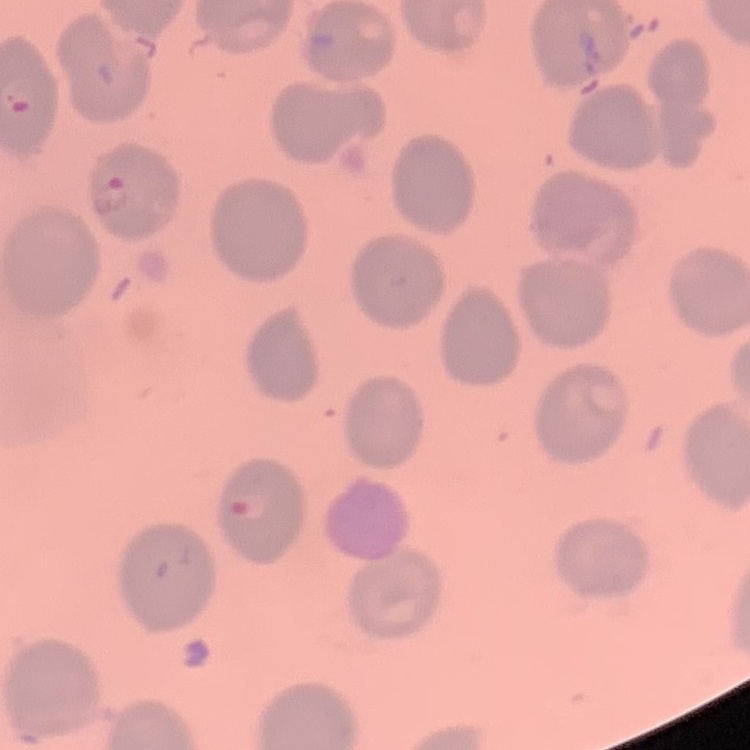
Summary:
  - Red blood cell morphology: no rouleaux formation
  - Preparation: thin blood film
  - Image type: square crop of a larger photomicrograph
  - Stain: Field's or Giemsa